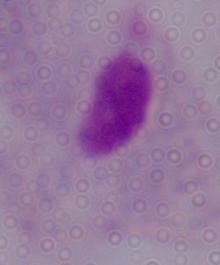

Summary:
  - Modality: micrograph
  - Magnification: 1000x
  - Identification: trichomonad